Classify this cell by malaria status.
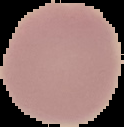

It is uninfected.

Image is 124×127 pixels. From a thin blood film. Cell region segmented out of the field of view; the surrounding area is masked to black.